Identify the blood parasite species.
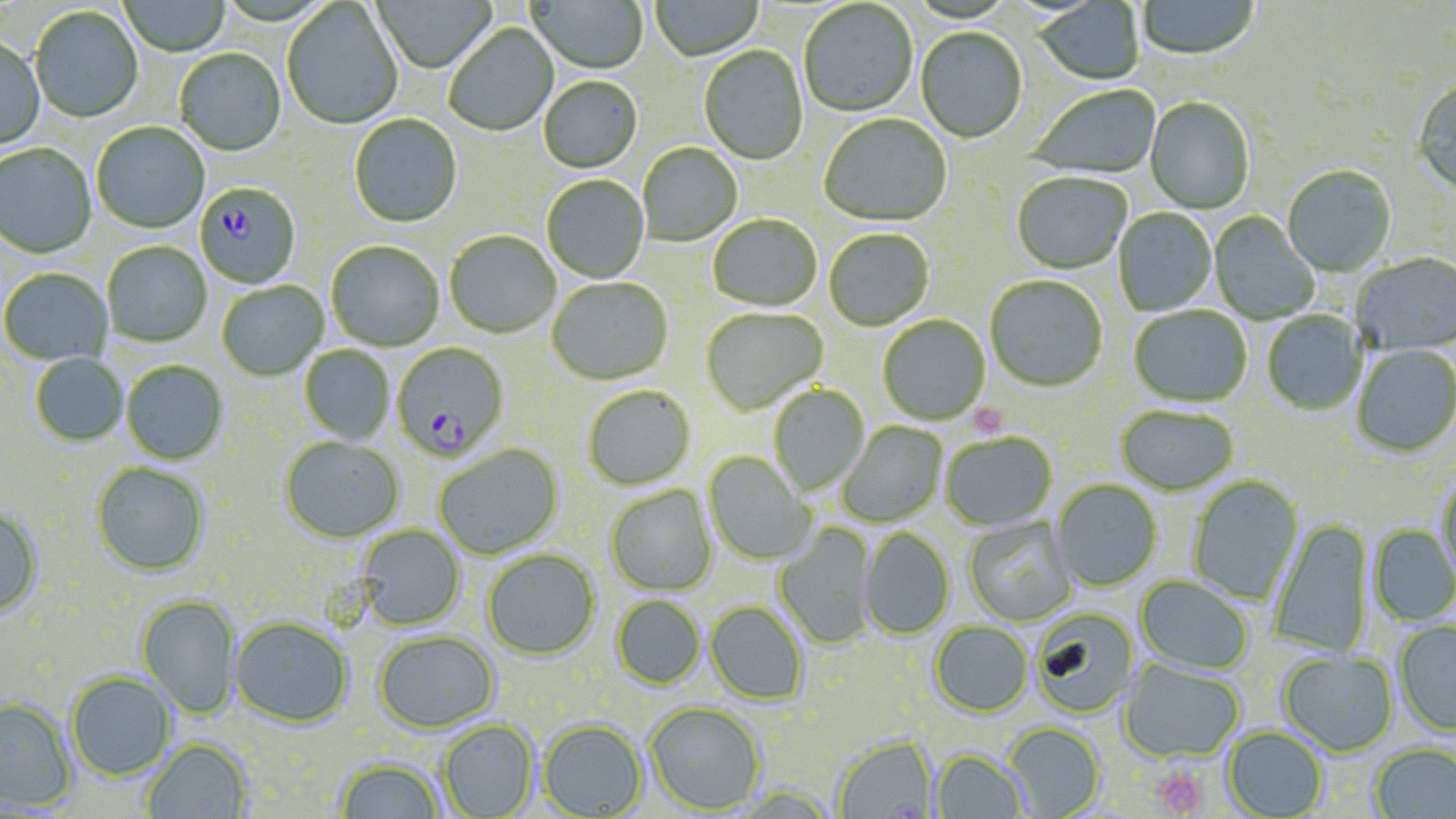

Plasmodium falciparum.

Approximate bounding boxes as (x1,y1)-(x2,y2) corner pairs in pixels. Plasmodium falciparum-infected red blood cell locations: (194,183)-(301,290), (391,344)-(510,462). Uninfected red blood cell locations: (372,0)-(497,75), (526,0)-(648,75), (118,1)-(232,57), (649,1)-(763,63), (1034,1)-(1144,86), (1137,1)-(1260,62), (282,2)-(404,130), (799,2)-(918,119), (30,7)-(143,124), (444,24)-(559,138), (915,28)-(1027,145), (0,38)-(45,152), (699,46)-(808,166), (175,50)-(286,158), (538,77)-(643,174), (1412,81)-(1456,195), (1028,85)-(1162,182), (1144,98)-(1254,216), (349,115)-(462,229), (819,115)-(952,228), (91,123)-(209,234), (0,144)-(97,260), (637,144)-(743,246), (1282,166)-(1396,278), (1012,174)-(1132,275), (542,176)-(649,283), (1113,208)-(1216,316), (1209,212)-(1320,325), (708,214)-(822,312), (824,229)-(934,332), (445,231)-(561,339), (102,241)-(211,347), (326,241)-(444,351), (1351,254)-(1456,356), (0,268)-(113,366), (985,276)-(1107,393), (546,278)-(673,386), (217,282)-(328,381), (1129,306)-(1252,408), (700,308)-(828,416), (1261,311)-(1367,416), (878,315)-(991,425), (1351,345)-(1456,458), (299,346)-(395,445), (30,353)-(129,446), (121,360)-(227,464), (768,384)-(869,497), (582,385)-(696,490), (1116,406)-(1238,496), (838,421)-(948,527), (940,433)-(1057,531), (280,435)-(404,543), (433,444)-(563,559), (704,452)-(815,566), (91,462)-(210,576), (1436,474)-(1456,586), (1187,475)-(1304,606), (1051,480)-(1162,592), (605,484)-(718,597), (0,505)-(44,619), (963,516)-(1077,626), (1268,519)-(1376,657), (773,522)-(877,650), (356,525)-(466,631), (1369,525)-(1456,626), (858,529)-(954,639), (482,550)-(599,660), (1135,576)-(1253,676), (136,595)-(241,718), (611,595)-(705,689), (705,602)-(809,705), (1030,608)-(1138,719), (230,616)-(354,728), (929,622)-(1033,717), (1394,622)-(1456,736), (374,631)-(499,733), (1278,652)-(1399,758), (1119,659)-(1245,763), (66,672)-(176,780), (0,697)-(77,811), (645,701)-(766,814), (438,719)-(538,818), (537,719)-(647,817), (1004,722)-(1105,818), (1222,727)-(1328,819), (832,735)-(938,819), (142,739)-(253,819), (1369,743)-(1456,819), (931,749)-(1030,818), (335,757)-(446,818). Platelet locations: (967,404)-(1009,438), (1150,764)-(1210,817). May-Grünwald-Giemsa-stained preparation. Thin blood film. Single field of view. 1000x magnification. Image is 1456×819 pixels. Light microscopy.